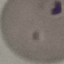
Summary:
  - Malaria status: parasitized
  - Preparation: thin blood smear
  - Stain: Giemsa
  - Capture: smartphone through the microscope eyepiece
  - Image type: automatically extracted cell patch, resized to 64 × 64 pixels